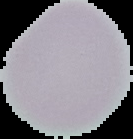

preparation = thin blood film
image size = 133×139 pixels
result = no malaria parasites detected
image type = cell region segmented out of the field of view; surrounding area masked to black